Report the malaria status of this cell.
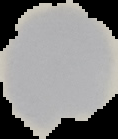

Uninfected.

From a thin blood film. Image is 118×139 pixels. The area outside the segmented cell region is set to black.